Describe the morphology of the red blood cells.
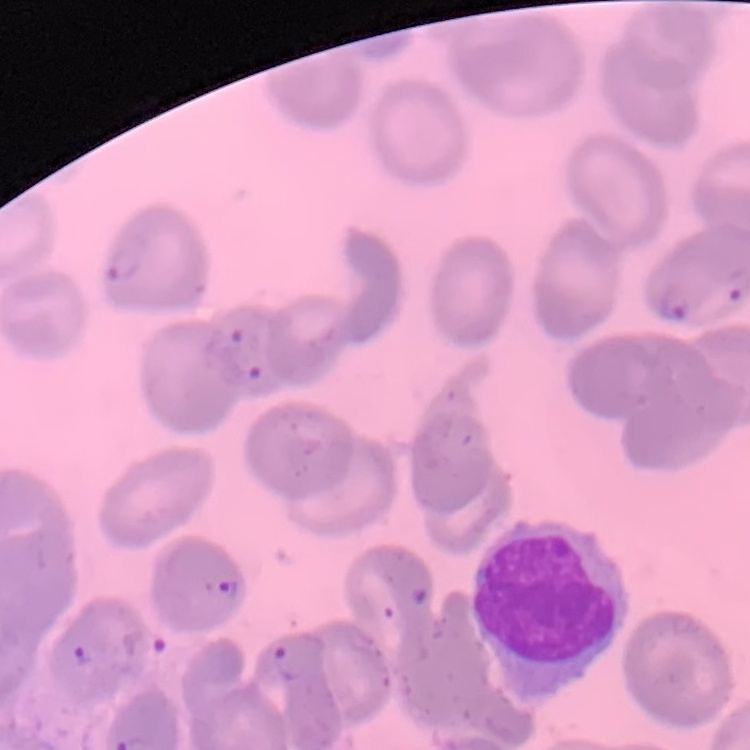

No rouleaux formation.

Field's or Giemsa stain. One tile cut from a larger photomicrograph. Thin blood film.